Give the extent of all Plasmodium vivax-infected red blood cells.
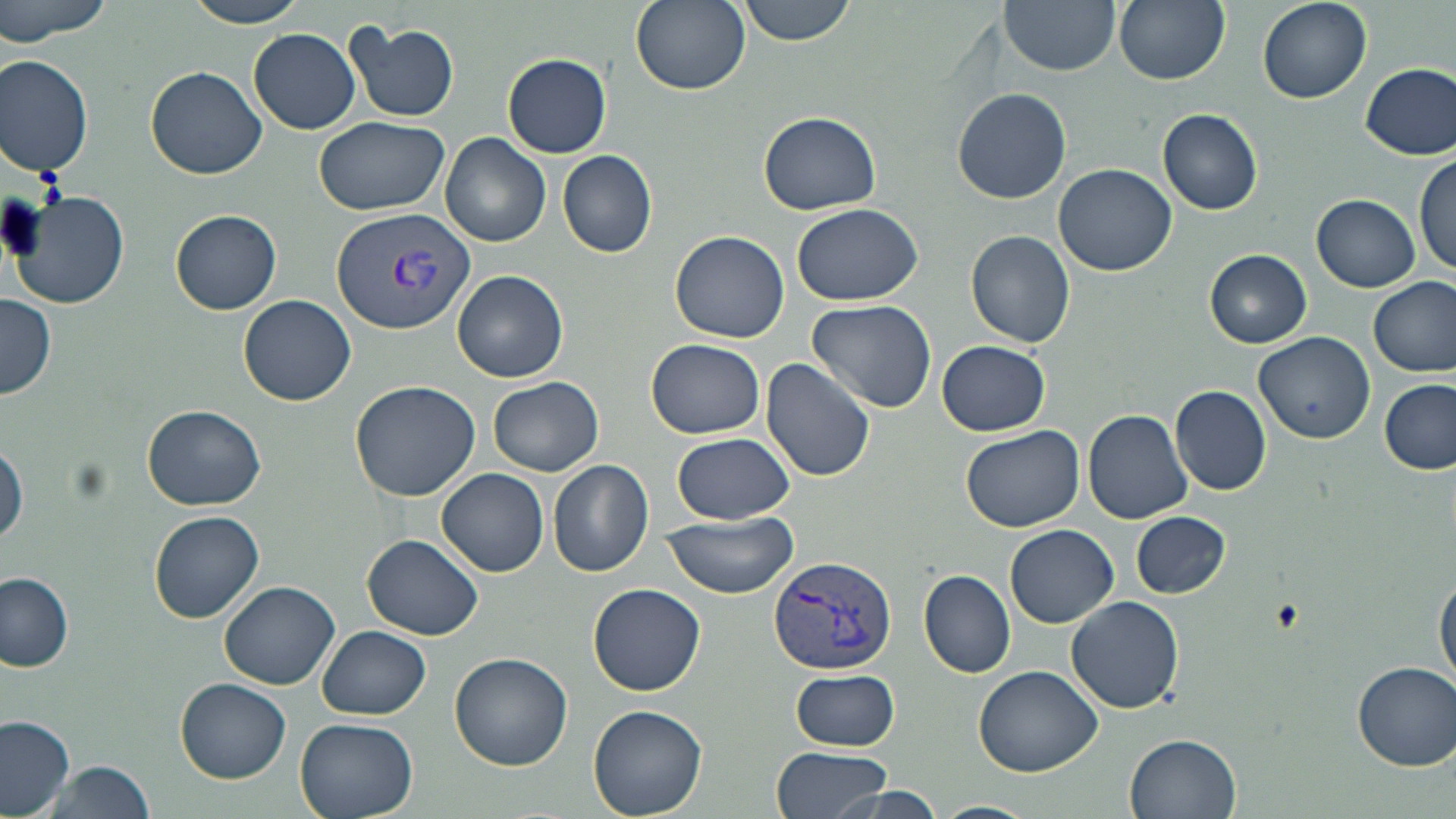

Approximate bounding boxes as [x1, y1, x2, y2] in pixels.
Plasmodium vivax-infected red blood cells: [332, 206, 477, 336], [767, 554, 898, 678].

Summary:
  - Uninfected red blood cell locations: [0, 0, 118, 44], [181, 0, 314, 27], [630, 0, 750, 96], [737, 0, 856, 46], [1001, 0, 1120, 75], [1113, 0, 1229, 86], [1256, 0, 1373, 104], [343, 20, 460, 123], [248, 28, 360, 134], [502, 53, 612, 158], [0, 55, 95, 175], [1362, 63, 1456, 159], [147, 66, 267, 179], [952, 87, 1071, 204], [1158, 108, 1263, 214], [758, 110, 884, 215], [314, 115, 450, 216], [441, 132, 552, 249], [558, 148, 658, 258], [1415, 154, 1455, 278], [1055, 164, 1175, 275], [9, 189, 131, 312], [1312, 194, 1420, 292], [793, 203, 923, 306], [169, 209, 282, 315], [670, 230, 789, 344], [966, 231, 1077, 347], [1205, 250, 1313, 348], [453, 269, 568, 384], [1370, 277, 1455, 376], [0, 293, 56, 399], [239, 294, 357, 406], [807, 299, 938, 415], [1256, 331, 1375, 443], [646, 338, 765, 439], [937, 339, 1051, 436], [761, 357, 878, 482], [489, 375, 604, 476], [1378, 377, 1456, 476], [348, 379, 479, 502], [1170, 385, 1272, 496], [144, 405, 264, 510], [1083, 409, 1192, 525], [960, 425, 1086, 532], [671, 431, 796, 524], [1, 439, 27, 549], [548, 460, 655, 578], [438, 469, 549, 576], [150, 511, 264, 622], [658, 511, 802, 597], [1131, 512, 1231, 599], [1006, 525, 1119, 629], [362, 534, 483, 640], [920, 570, 1017, 677], [1433, 570, 1455, 690], [0, 571, 75, 671], [220, 580, 340, 690], [589, 584, 705, 694], [1065, 596, 1185, 714], [316, 626, 431, 718], [450, 652, 573, 772], [1352, 660, 1455, 770], [974, 665, 1102, 776], [788, 667, 901, 751], [174, 678, 291, 783], [589, 705, 707, 817], [0, 713, 77, 816], [295, 716, 419, 819], [1126, 733, 1240, 818], [771, 745, 894, 819], [38, 758, 156, 819], [823, 786, 953, 818], [933, 799, 1037, 819]
  - Slide-level diagnosis: Plasmodium vivax
  - Stain: May-Grünwald-Giemsa
  - Modality: optical microscopy
  - Magnification: 1000x
  - Field of view: one of a larger specimen
  - Image size: 1456×819 pixels
  - Preparation: thin blood film